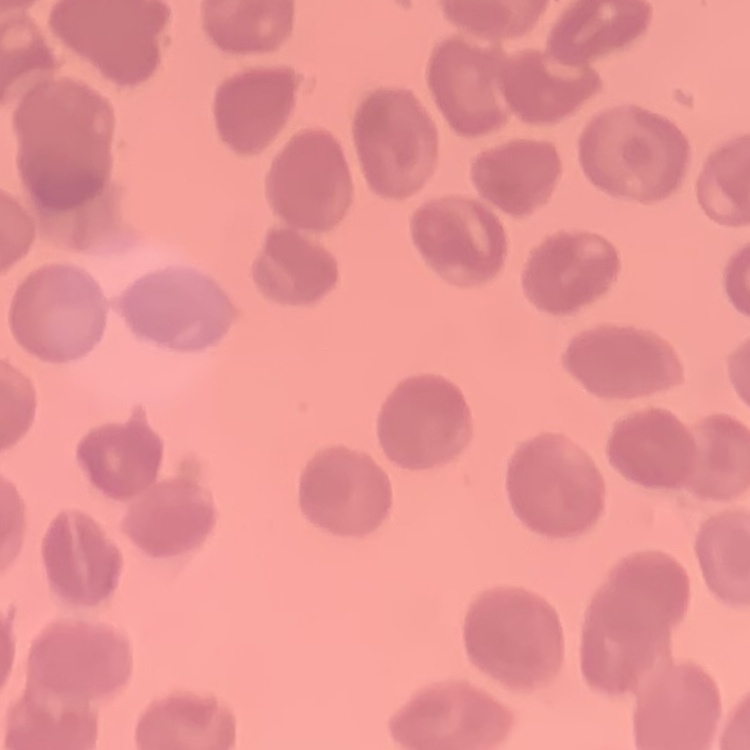

Summary:
  - Red blood cell morphology: no rouleaux formation
  - Stain: Field's or Giemsa
  - Preparation: thin peripheral smear
  - Image type: square crop of a larger photomicrograph